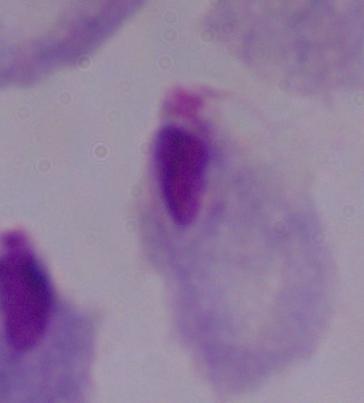

{
  "modality": "photomicrograph",
  "identification": "trichomonad",
  "magnification": "1000x"
}